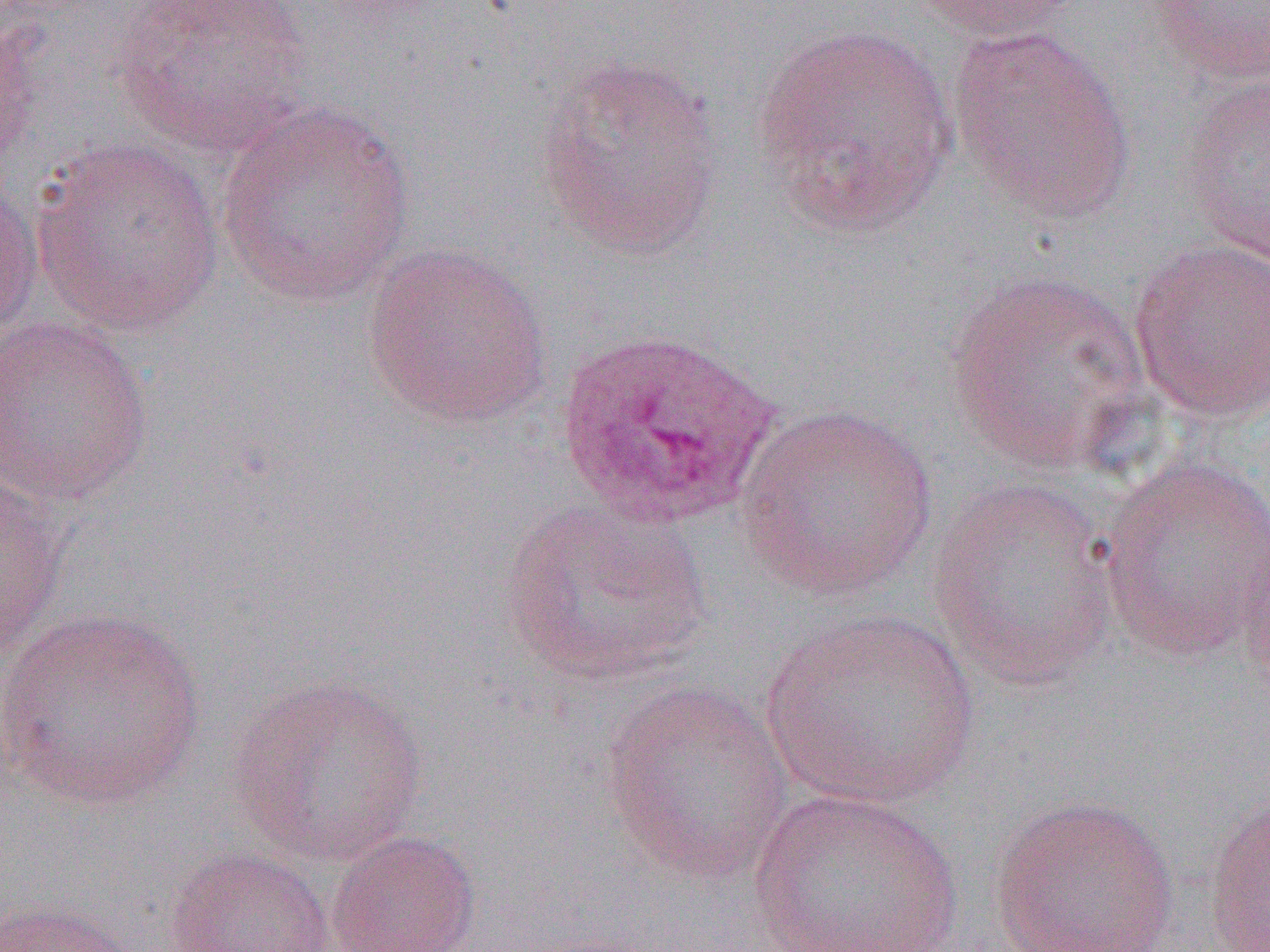
slide-level diagnosis = Plasmodium ovale
image size = 1270×952 pixels
modality = optical microscopy
magnification = 1000x
Plasmodium ovale-infected red blood cell locations = approximate bounding boxes as (x1,y1)-(x2,y2) corner pairs in pixels: (557,327)-(779,530)
preparation = thin blood smear
field of view = one of a larger specimen
uninfected red blood cell locations = approximate bounding boxes as (x1,y1)-(x2,y2) corner pairs in pixels: (110,0)-(318,156), (908,0)-(1089,41), (1146,0)-(1270,85), (1,10)-(50,172), (751,21)-(960,240), (947,25)-(1137,223), (532,53)-(728,263), (1180,74)-(1270,265), (214,101)-(417,308), (31,136)-(226,337), (0,173)-(43,341), (1129,240)-(1270,423), (362,241)-(554,431), (945,269)-(1154,476), (1,316)-(155,505), (734,402)-(940,601), (1097,455)-(1270,663), (0,471)-(68,661), (929,477)-(1122,692), (498,495)-(713,687), (1235,519)-(1270,717), (0,606)-(208,812), (758,607)-(982,812), (224,674)-(431,867), (598,679)-(795,885), (746,787)-(965,952), (1203,792)-(1270,951), (987,793)-(1182,952), (325,830)-(482,952), (163,846)-(335,952), (0,897)-(149,952)